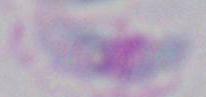

Summary:
  - Modality: photomicrograph
  - Magnification: 1000x
  - Identification: Toxoplasma gondii